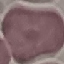

Summary:
  - Result: no malaria parasites detected
  - Preparation: thin blood smear
  - Capture: smartphone camera at the microscope eyepiece
  - Stain: Giemsa
  - Image type: cell patch, automatically extracted from a larger field of view and resized to 64 × 64 pixels